Classify this cell by malaria status.
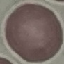

Uninfected.

Summary:
  - Preparation: thin blood film
  - Capture: smartphone through the microscope eyepiece
  - Stain: Giemsa
  - Image type: cell patch, automatically extracted from a larger field of view and resized to 64 × 64 pixels